State which cell type is depicted.
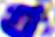
A leukocyte.

Summary:
  - Magnification: 400x
  - Modality: micrograph